Name the parasite shown.
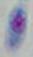
This is Toxoplasma gondii.

Summary:
  - Modality: micrograph
  - Magnification: 1000x